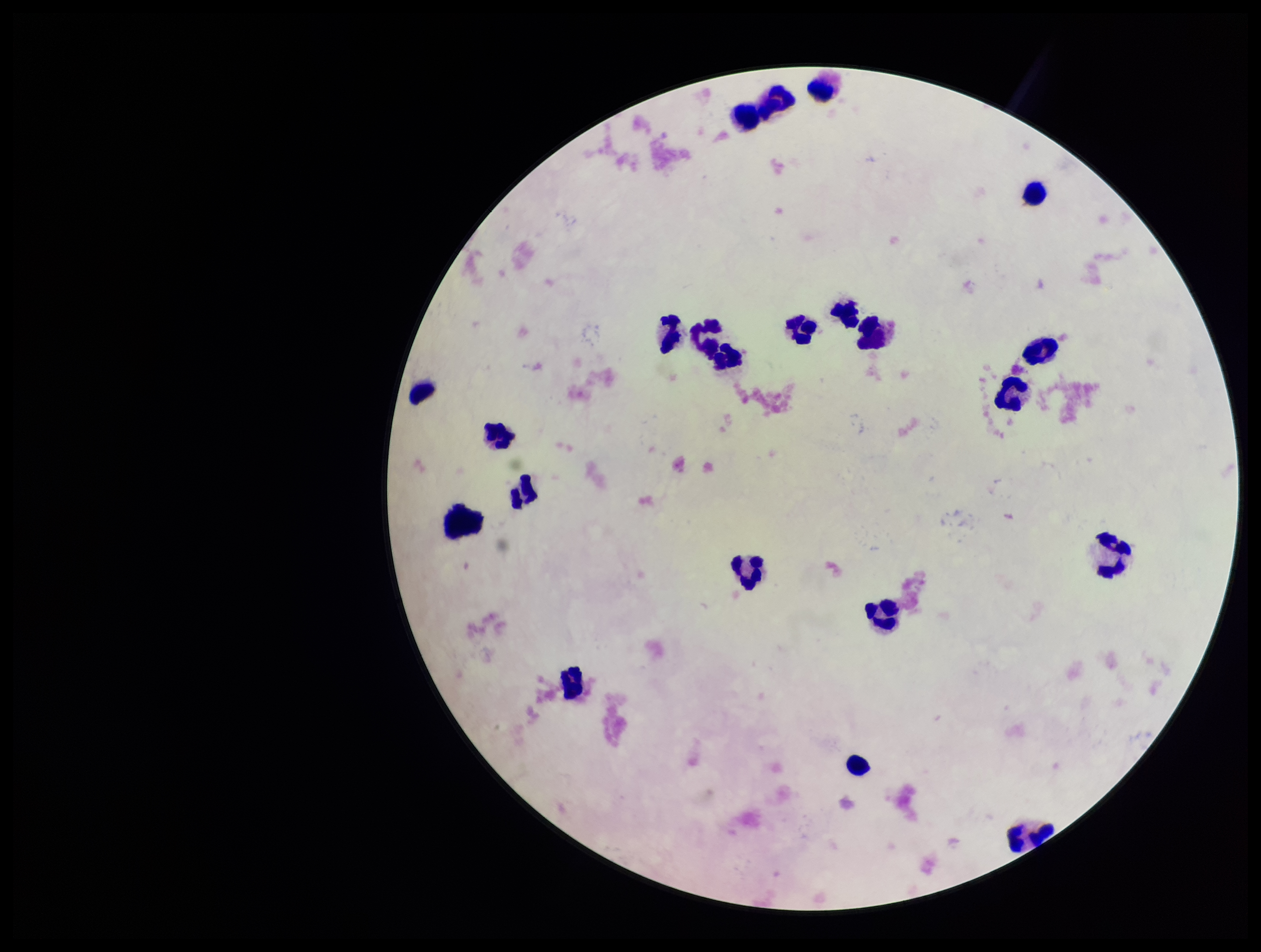
Summary:
  - Parasite count: 0
  - Capture: smartphone photograph through the microscope eyepiece
  - Image size: 1261×952 pixels
  - Stain: Giemsa
  - Patient malaria status: negative
  - Preparation: thick smear
  - Plasmodium parasites: none identified
  - Leukocyte count: 21
  - Field of view: one from this slide